Give the extent of all Plasmodium ovale-infected red blood cells.
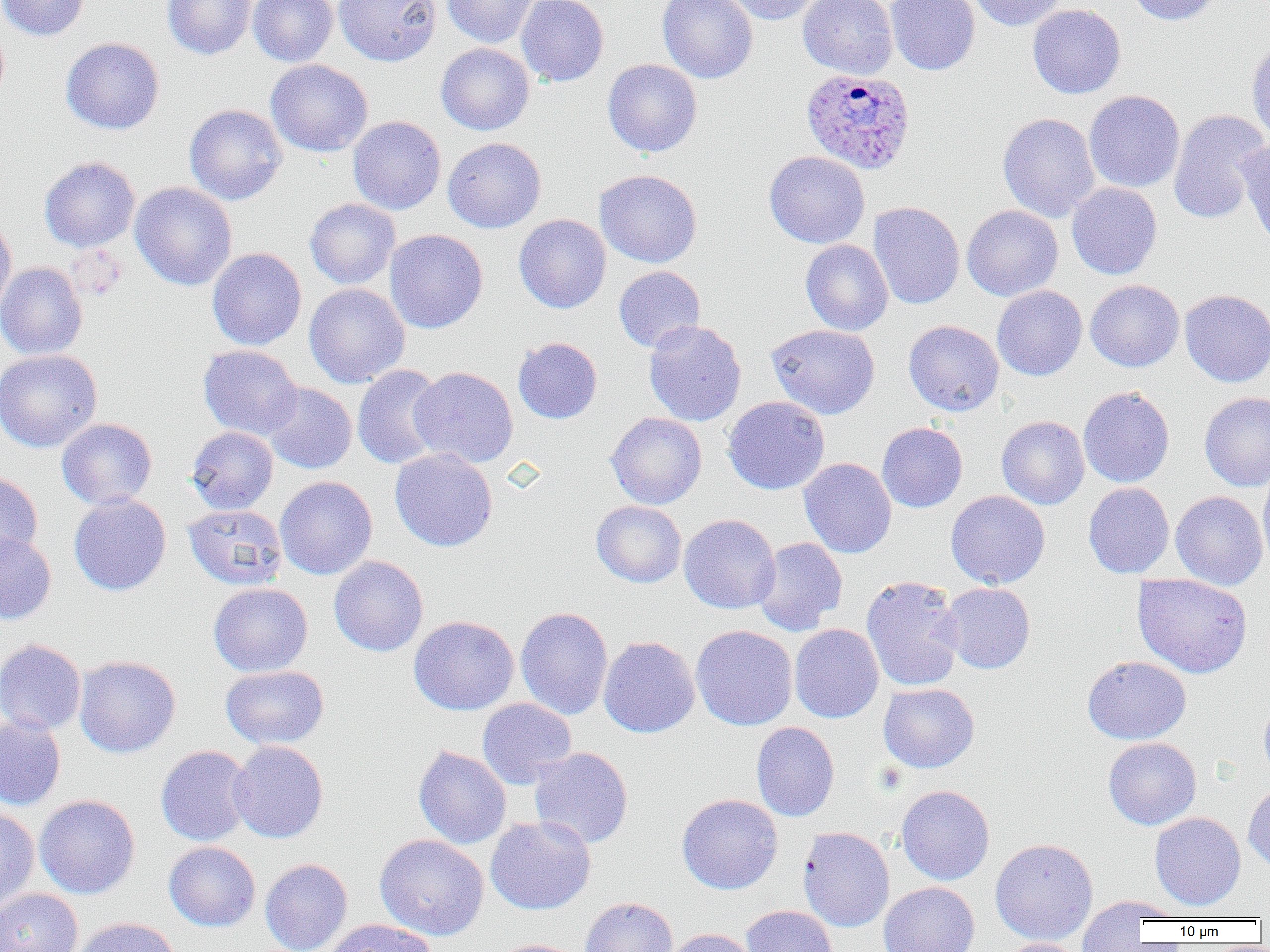

Approximate bounding boxes as (x1, y1, x2, y2) in pixels.
Plasmodium ovale-infected red blood cells: (800, 68, 917, 175).

slide-level diagnosis = Plasmodium ovale
uninfected red blood cell locations = approximate bounding boxes as (x1, y1, x2, y2) in pixels: (0, 0, 91, 41), (162, 0, 256, 60), (248, 0, 337, 67), (335, 0, 440, 66), (443, 0, 539, 48), (516, 0, 609, 87), (657, 0, 758, 84), (721, 0, 824, 25), (798, 0, 898, 79), (886, 0, 980, 76), (966, 0, 1068, 31), (1126, 0, 1222, 26), (1027, 3, 1126, 99), (1246, 35, 1270, 145), (60, 37, 165, 135), (435, 43, 535, 135), (265, 59, 373, 156), (602, 59, 702, 157), (1084, 90, 1185, 193), (184, 104, 287, 205), (1168, 109, 1269, 224), (997, 112, 1100, 222), (347, 116, 446, 214), (443, 137, 546, 233), (1237, 138, 1270, 249), (764, 151, 870, 249), (39, 156, 140, 252), (594, 169, 702, 268), (130, 182, 237, 290), (1067, 183, 1162, 279), (304, 198, 401, 289), (867, 201, 965, 310), (962, 205, 1063, 301), (514, 214, 611, 314), (0, 217, 17, 319), (385, 229, 488, 333), (800, 240, 893, 336), (207, 248, 306, 350), (0, 262, 88, 360), (613, 266, 706, 353), (1085, 280, 1184, 372), (304, 283, 410, 387), (992, 285, 1087, 381), (1180, 289, 1270, 387), (644, 320, 746, 426), (903, 320, 1004, 416), (766, 324, 880, 419), (513, 337, 603, 424), (198, 344, 302, 440), (0, 349, 102, 452), (352, 364, 446, 470), (408, 367, 518, 467), (263, 383, 357, 474), (1078, 387, 1175, 488), (1199, 391, 1270, 492), (723, 396, 830, 495), (606, 412, 707, 509), (996, 416, 1089, 509), (56, 418, 157, 509), (876, 422, 968, 513), (186, 426, 278, 515), (390, 448, 498, 552), (798, 457, 897, 558), (1257, 465, 1270, 575), (0, 471, 43, 564), (275, 476, 377, 579), (1083, 482, 1175, 579), (946, 490, 1050, 589), (1170, 491, 1268, 590), (68, 493, 171, 596), (591, 500, 687, 588), (183, 504, 287, 589), (679, 513, 781, 614), (0, 532, 56, 624), (752, 538, 848, 636), (329, 556, 428, 656), (1132, 573, 1253, 678), (861, 575, 964, 691), (208, 582, 313, 677), (940, 582, 1036, 674), (515, 606, 613, 720), (408, 616, 519, 715), (789, 623, 884, 723), (691, 625, 798, 730), (598, 635, 700, 738), (0, 638, 87, 735), (74, 655, 181, 757), (1082, 655, 1192, 744), (220, 665, 329, 749), (878, 683, 980, 773), (477, 698, 576, 789), (1259, 698, 1270, 784), (0, 714, 66, 810), (751, 722, 840, 821), (1103, 737, 1201, 830), (228, 740, 329, 844), (155, 745, 254, 847), (413, 745, 511, 849), (528, 746, 633, 849), (1243, 782, 1270, 873), (896, 785, 995, 885), (676, 793, 783, 894), (35, 794, 140, 899), (0, 807, 40, 912), (1149, 812, 1246, 910), (485, 815, 596, 915), (798, 826, 895, 932), (375, 834, 489, 940), (990, 838, 1098, 944), (163, 841, 260, 931), (260, 858, 352, 952), (878, 882, 979, 952), (0, 888, 83, 952), (580, 896, 678, 952), (1085, 896, 1186, 922), (1076, 897, 1168, 949), (740, 905, 839, 952), (72, 917, 182, 952), (323, 919, 437, 952), (662, 928, 758, 952), (491, 938, 587, 952), (997, 938, 1087, 952)
image size = 1270×952 pixels
preparation = thin blood smear
modality = light microscopy
field of view = one of a larger specimen
magnification = 1000x